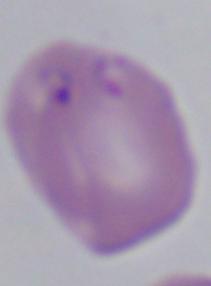

A Babesia parasite is seen. Photomicrograph. Captured at 1000x magnification.